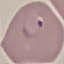

Malaria status: parasitized. Acquired by smartphone through the microscope eyepiece. Giemsa stain. Automatically extracted cell patch, resized to 64 × 64 pixels. Thin blood smear.